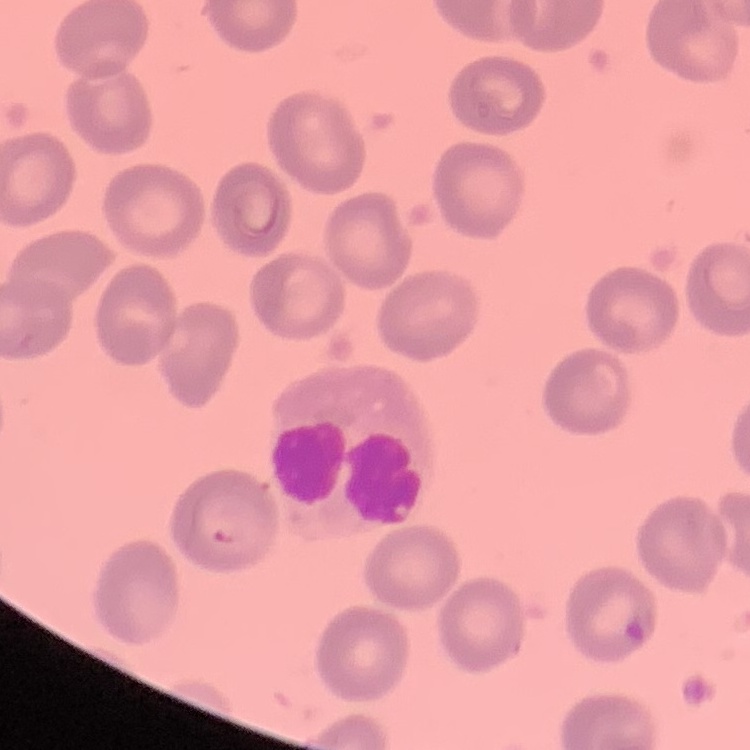

The red blood cells show no rouleaux formation. Stained with either Field's or Giemsa. Thin blood smear. Square crop of a larger photomicrograph.